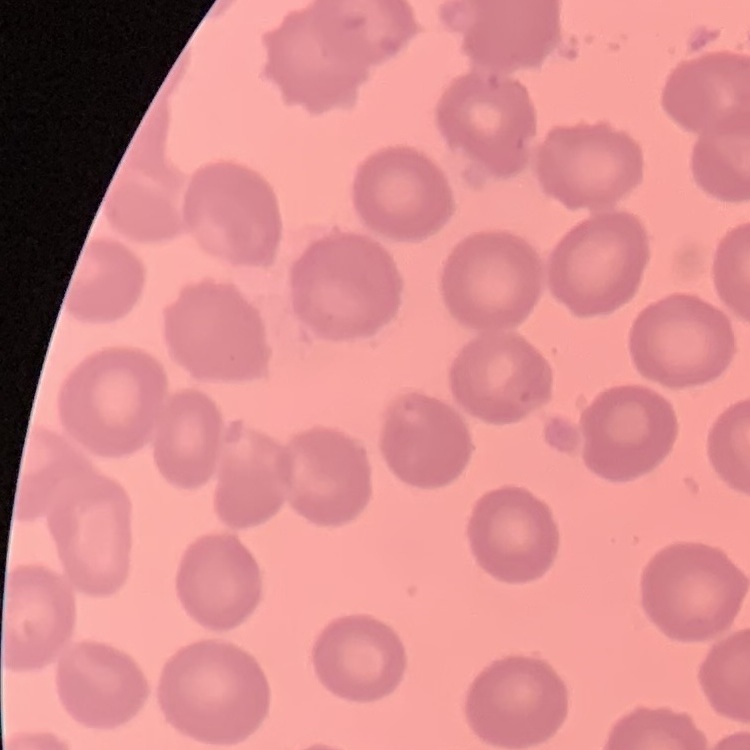
The red blood cells show no rouleaux formation. Thin peripheral smear. One tile cut from a larger photomicrograph. Field's or Giemsa stain.